Classify this cell by malaria status.
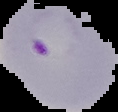
It is parasitized.

Summary:
  - Image type: segmented cell region on a black background
  - Preparation: thin blood film
  - Image size: 118×112 pixels